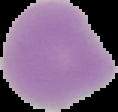
preparation = thin blood film
image type = segmented cell region on a black background
image size = 118×112 pixels
malaria status = uninfected